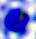
A leukocyte is seen. Micrograph. Captured at 400x magnification.